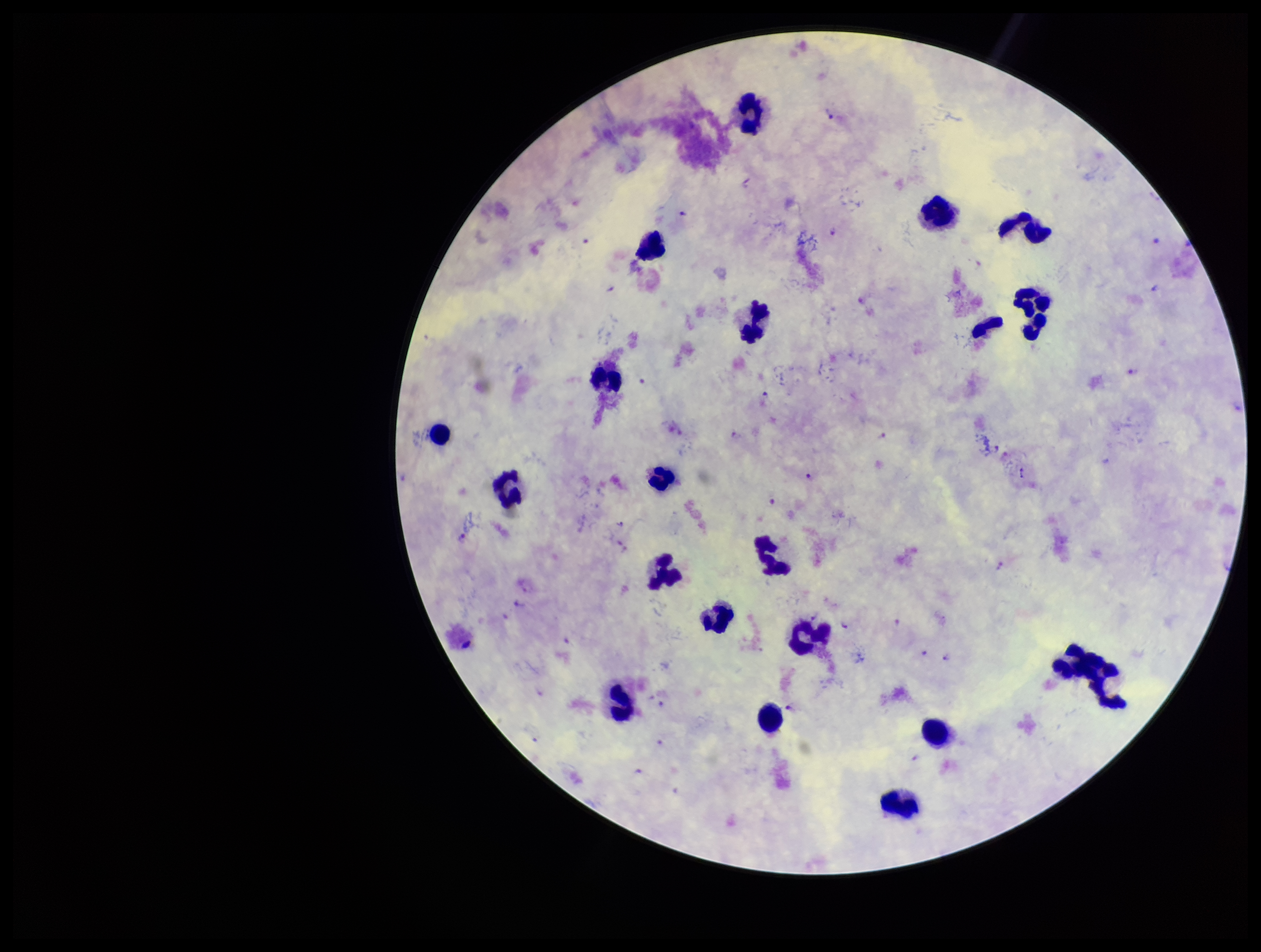
patient malaria status = infected
Plasmodium parasites = seen
parasite count = 21
image size = 1261×952 pixels
field of view = one from this slide
preparation = thick smear
species reported for this patient = Plasmodium falciparum
leukocyte count = 19
capture = smartphone photograph through the microscope eyepiece
stain = Giemsa